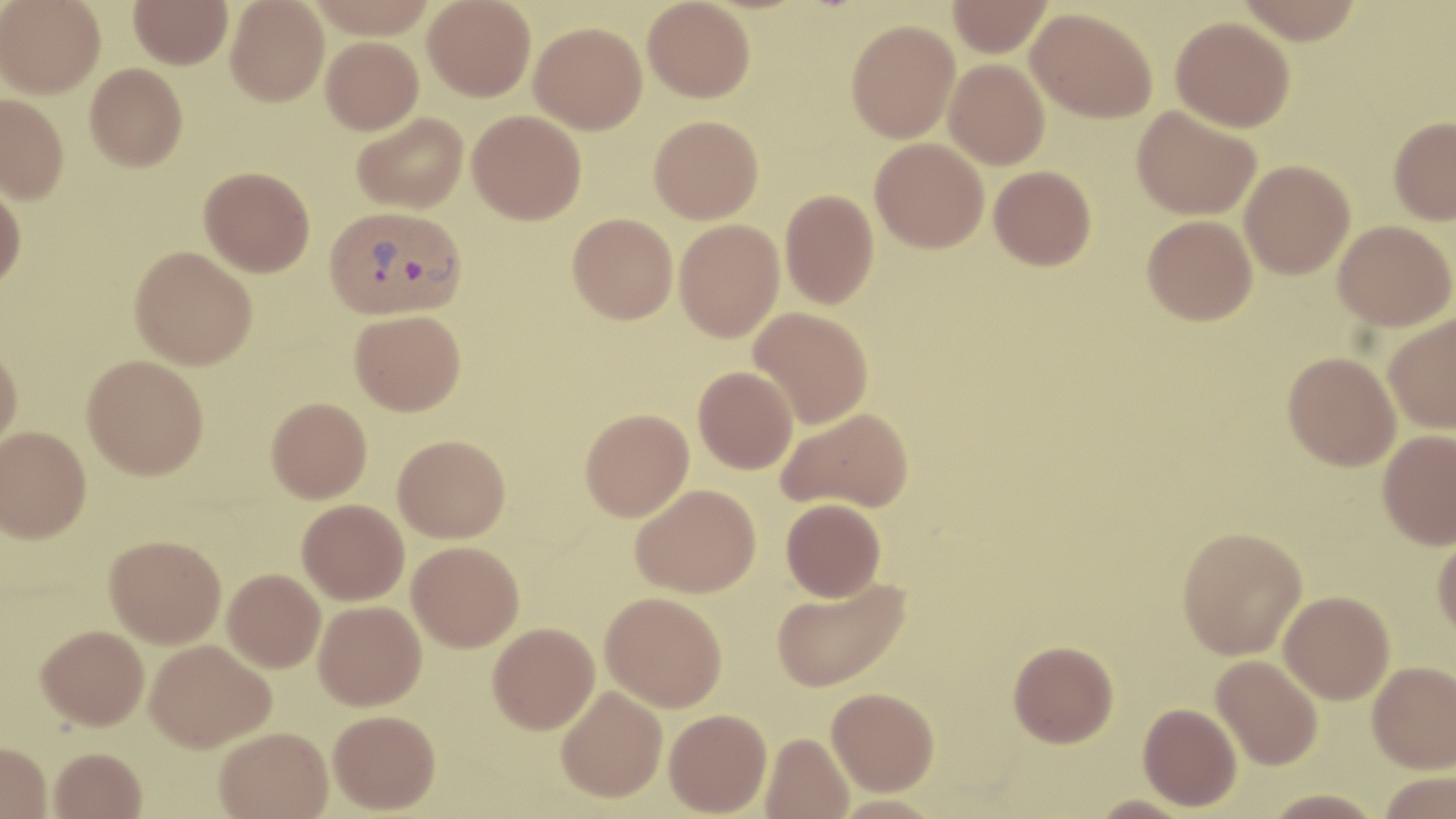

{
  "slide_level_diagnosis": "Plasmodium vivax",
  "field_of_view": "one of a larger specimen",
  "stain": "May-Grünwald-Giemsa",
  "plasmodium_vivax_infected_red_blood_cell_locations": "approximate bounding boxes as (x1,y1)-(x2,y2) corner pairs in pixels: (324,204)-(466,320)",
  "image_size": "1456×819 pixels",
  "magnification": "1000x",
  "modality": "optical microscopy",
  "preparation": "thin blood film",
  "uninfected_red_blood_cell_locations": "approximate bounding boxes as (x1,y1)-(x2,y2) corner pairs in pixels: (1,0)-(105,97), (129,0)-(232,69), (226,0)-(329,106), (423,0)-(535,101), (642,0)-(755,102), (947,0)-(1052,57), (1236,0)-(1366,44), (1026,7)-(1157,123), (1171,16)-(1295,132), (846,19)-(960,142), (530,22)-(647,134), (320,36)-(423,135), (944,58)-(1050,169), (85,63)-(188,171), (0,94)-(69,204), (1132,105)-(1261,220), (467,110)-(586,224), (352,112)-(468,213), (649,115)-(763,223), (1388,116)-(1456,224), (870,137)-(989,252), (1240,160)-(1354,279), (989,165)-(1096,270), (199,166)-(315,276), (0,183)-(26,290), (780,189)-(879,308), (567,213)-(678,324), (1142,214)-(1257,325), (674,218)-(784,341), (1334,220)-(1455,331), (130,246)-(257,369), (749,307)-(873,428), (350,310)-(466,416), (1383,313)-(1456,434), (0,344)-(22,452), (1282,352)-(1400,470), (82,354)-(209,479), (693,365)-(798,474), (267,397)-(372,503), (778,407)-(914,513), (580,408)-(694,521), (1,426)-(91,542), (1378,430)-(1456,549), (393,434)-(510,542), (631,483)-(761,597), (781,498)-(886,601), (297,499)-(409,605), (1177,525)-(1308,659), (1433,529)-(1456,641), (105,535)-(226,648), (407,541)-(524,651), (223,568)-(325,672), (771,576)-(911,692), (1279,591)-(1395,704), (600,592)-(727,711), (314,600)-(426,710), (487,622)-(600,734), (36,624)-(149,729), (145,640)-(275,752), (1008,640)-(1119,747), (1212,654)-(1324,770), (1367,661)-(1456,773), (556,685)-(668,802), (827,687)-(939,795), (1138,702)-(1242,811), (664,708)-(772,816), (328,709)-(441,813), (214,726)-(333,818), (761,732)-(854,819), (0,740)-(52,818), (49,747)-(146,819), (1379,771)-(1455,818), (1262,788)-(1385,819), (1087,794)-(1198,819)"
}